Name the parasite shown.
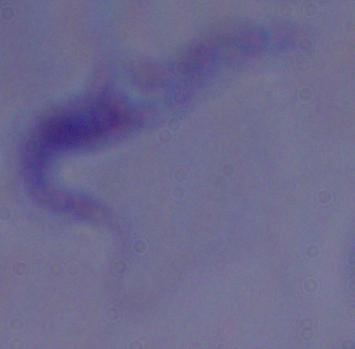

A trypanosome.

Summary:
  - Magnification: 1000x
  - Modality: micrograph